Outline each blood parasite and name the species.
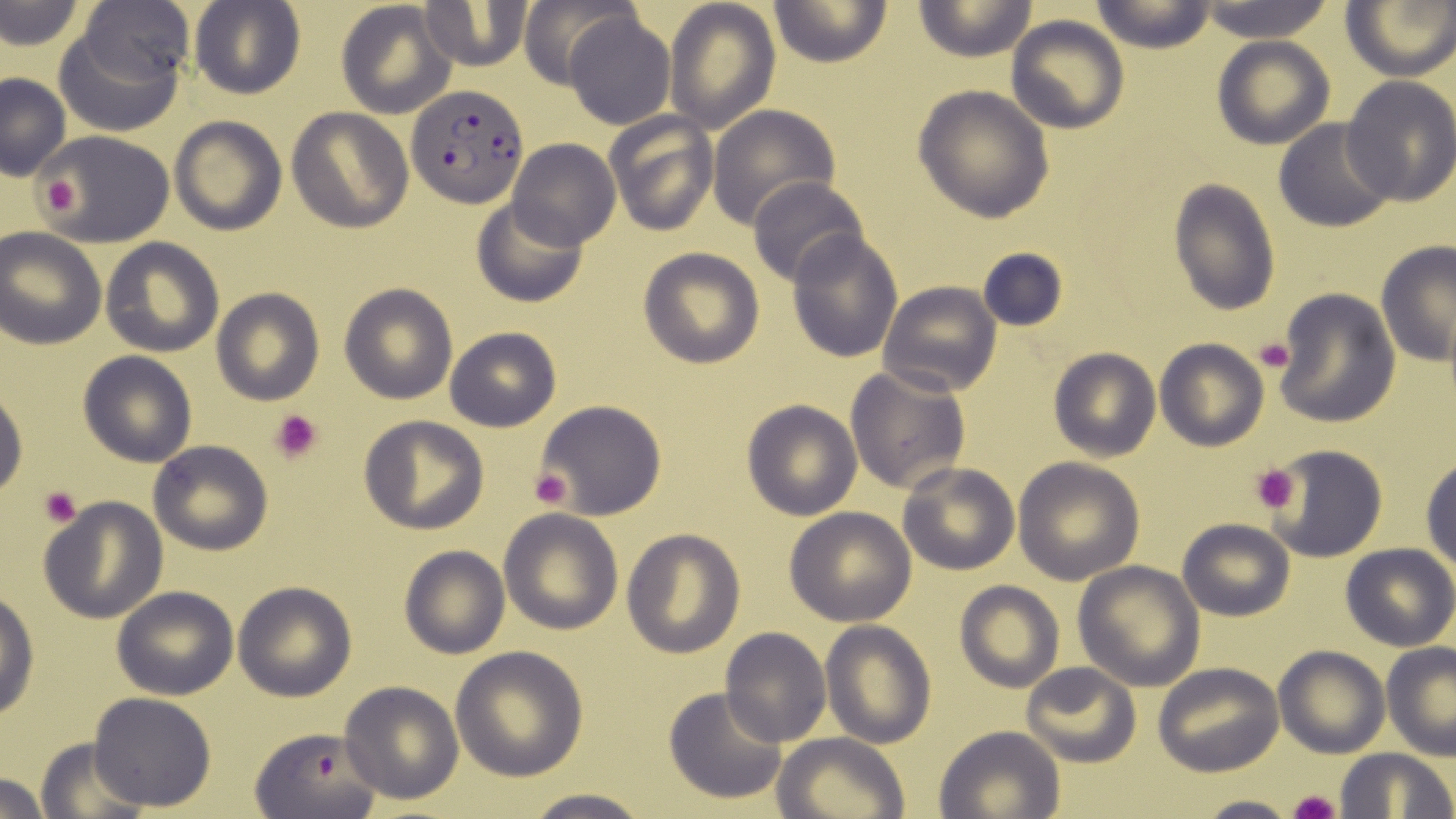
Approximate bounding boxes as (x1,y1)-(x2,y2) corner pairs in pixels.
Plasmodium falciparum-infected red blood cells: (407,85)-(528,208), (249,723)-(381,817).
No Plasmodium ovale, Plasmodium malariae, Plasmodium vivax, Babesia divergens, or Trypanosoma brucei observed.

Summary:
  - Platelet locations: (36,170)-(83,221), (1254,338)-(1295,373), (269,408)-(323,464), (1249,462)-(1300,512), (529,469)-(573,510), (40,486)-(84,529), (1290,790)-(1342,819)
  - Uninfected red blood cell locations: (664,0)-(781,134), (771,0)-(891,68), (1089,0)-(1219,53), (1339,0)-(1455,81), (2,1)-(84,48), (189,1)-(306,100), (334,1)-(457,119), (420,1)-(535,71), (913,1)-(1039,63), (77,2)-(196,88), (518,2)-(633,87), (1193,2)-(1339,42), (564,10)-(675,129), (53,16)-(184,137), (1006,16)-(1129,133), (1212,35)-(1336,150), (0,73)-(71,182), (1339,75)-(1456,208), (913,87)-(1054,223), (707,104)-(841,229), (287,108)-(413,233), (605,111)-(719,235), (169,116)-(286,235), (1272,120)-(1396,233), (30,128)-(178,248), (507,139)-(620,251), (748,178)-(871,289), (1168,179)-(1281,318), (471,196)-(591,308), (0,229)-(105,348), (787,230)-(904,362), (101,238)-(224,357), (1376,243)-(1456,369), (976,245)-(1071,333), (639,248)-(764,368), (880,281)-(1002,398), (338,282)-(458,404), (210,288)-(324,405), (1272,288)-(1401,428), (445,327)-(561,431), (1155,339)-(1268,450), (1049,348)-(1160,461), (78,350)-(197,468), (844,364)-(972,495), (0,379)-(28,500), (537,398)-(666,520), (741,398)-(863,520), (359,417)-(488,534), (147,439)-(273,554), (1269,444)-(1387,561), (1013,457)-(1145,584), (1421,459)-(1455,571), (897,461)-(1019,575), (37,495)-(168,625), (786,505)-(916,626), (499,509)-(623,634), (1178,518)-(1294,621), (621,527)-(746,658), (1340,542)-(1456,651), (398,545)-(510,659), (1072,559)-(1206,690), (232,579)-(357,702), (954,579)-(1064,693), (111,585)-(240,699), (0,589)-(38,720), (821,620)-(935,749), (721,628)-(831,747), (1381,642)-(1456,759), (1273,646)-(1389,757), (450,647)-(589,780), (1021,663)-(1142,766), (1154,663)-(1283,777), (339,680)-(463,804), (663,687)-(790,805), (87,692)-(217,809), (934,725)-(1065,818), (774,731)-(909,819), (34,736)-(148,816), (1335,747)-(1455,818), (0,772)-(55,818), (516,789)-(655,819), (1190,794)-(1302,819)
  - Slide-level diagnosis: Plasmodium falciparum
  - Modality: light microscopy
  - Magnification: 1000x
  - Field of view: one of a larger specimen
  - Preparation: thin blood film
  - Image size: 1456×819 pixels
  - Stain: May-Grünwald-Giemsa